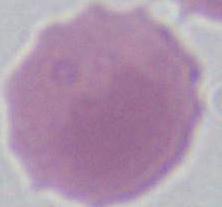

Photomicrograph. An erythrocyte is shown. Captured at 1000x magnification.